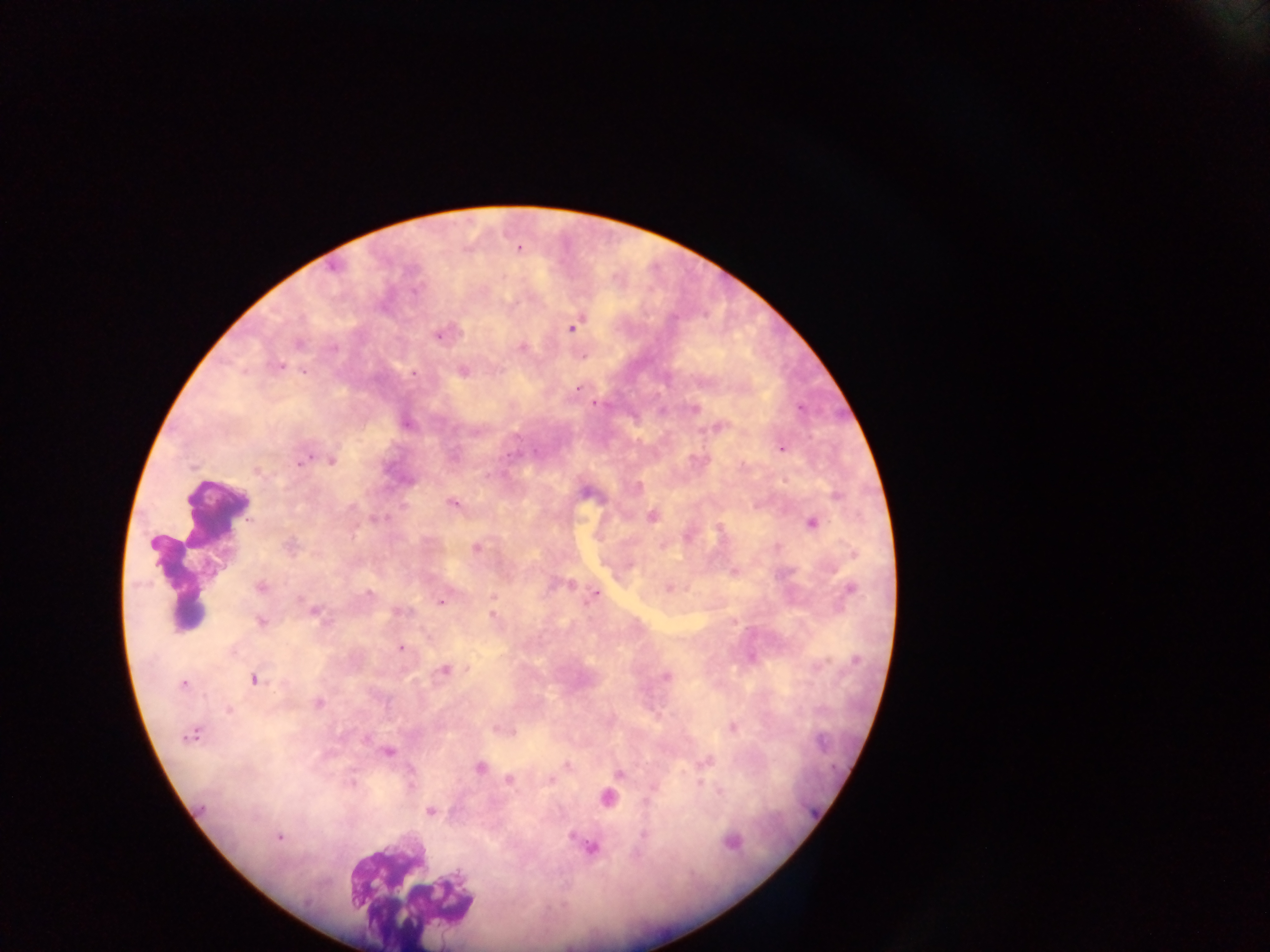
capture: mobile-phone photograph through a microscope
image_size: 1270×952 pixels
country: Ghana
malaria_parasite_locations: 'approximate centers as [x, y] in pixels: [519, 249], [571, 328], [439, 334], [298, 344], [522, 348], [279, 366], [303, 371], [463, 372], [413, 374], [578, 388], [595, 404], [800, 408], [694, 409], [407, 424], [718, 428], [782, 449], [307, 458], [332, 460], [300, 462], [257, 471], [837, 497], [452, 503], [351, 507], [651, 516], [812, 524], [153, 543], [289, 546], [476, 547], [853, 554], [571, 584], [259, 587], [669, 587], [850, 589], [368, 594], [596, 594], [493, 597], [442, 602], [314, 611], [401, 611], [492, 616], [260, 622], [400, 648], [856, 660], [444, 670], [667, 676], [253, 680], [183, 684], [318, 703], [228, 710], [732, 728], [191, 735], [366, 739], [387, 752], [567, 766], [480, 768], [619, 774], [509, 780], [550, 780], [351, 784], [719, 792], [606, 797], [430, 811], [643, 835], [279, 837], [731, 842], [592, 847]'
preparation: thick blood smear
field_of_view: single
leukocyte_locations: 'approximate centers as [x, y] in pixels: [213, 509], [408, 891]'